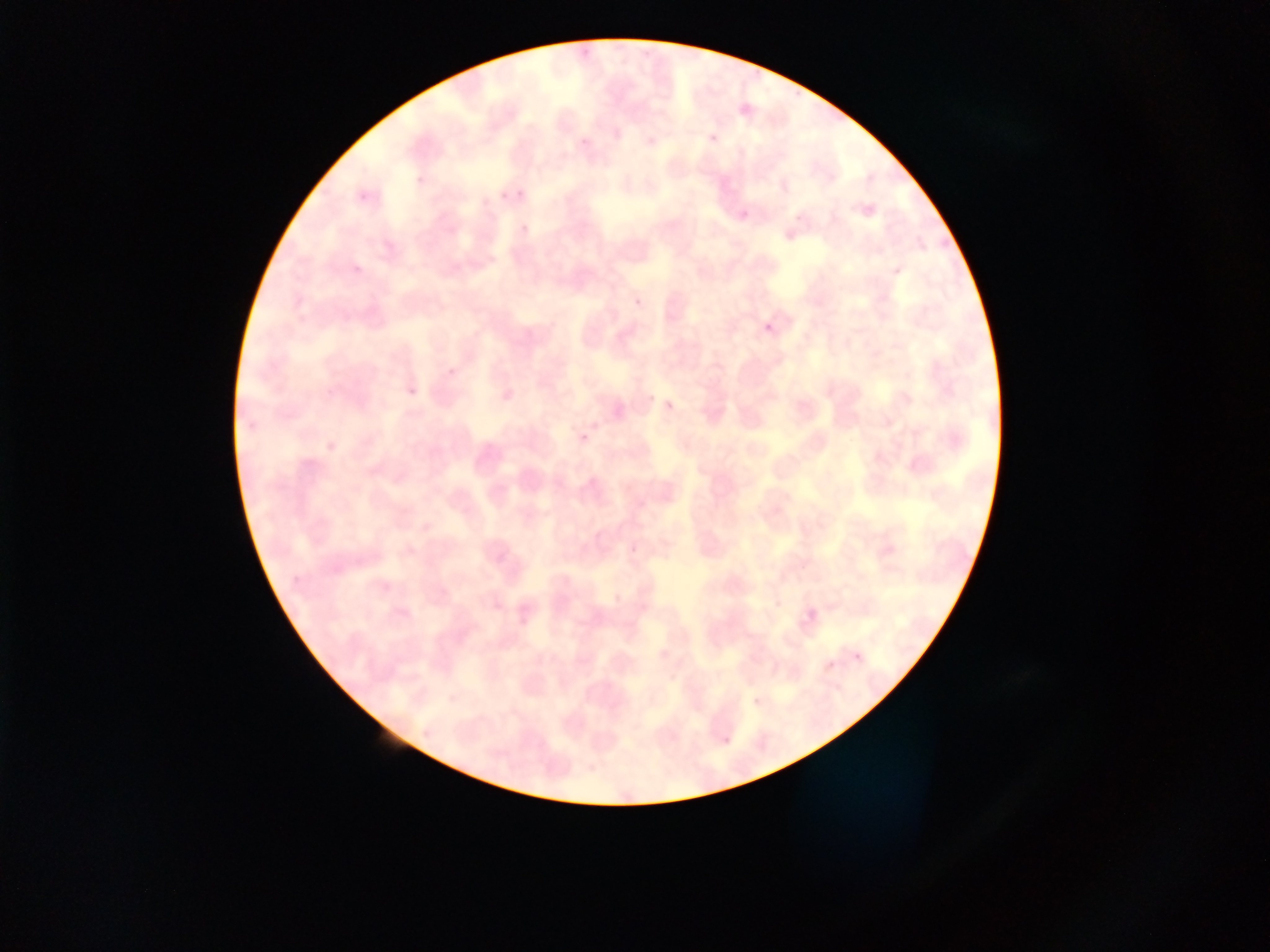
Approximate bounding boxes as left top right bottom in pixels. Malaria parasite locations: 736 98 760 124; 512 190 525 201; 497 192 505 202; 737 201 752 218; 518 221 531 235; 632 294 647 311; 758 316 784 344; 445 364 459 379; 405 389 416 400; 659 394 682 417; 574 426 598 451; 797 604 826 635. One field of view. Photographed through a microscope with a mobile-phone camera. Thin blood film. Image is 1270×952 pixels. Sample from Ghana.